Identify the parasite.
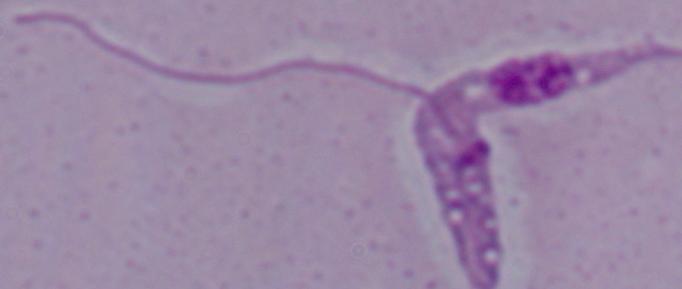

This is Leishmania.

modality: photomicrograph
magnification: 1000x